Name the cell type shown.
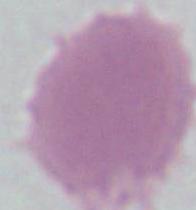
This is an erythrocyte.

Micrograph. 1000x magnification.